Identify the parasite.
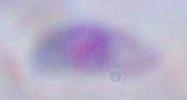
This is Toxoplasma gondii.

modality = micrograph
magnification = 1000x